Give the preparation type.
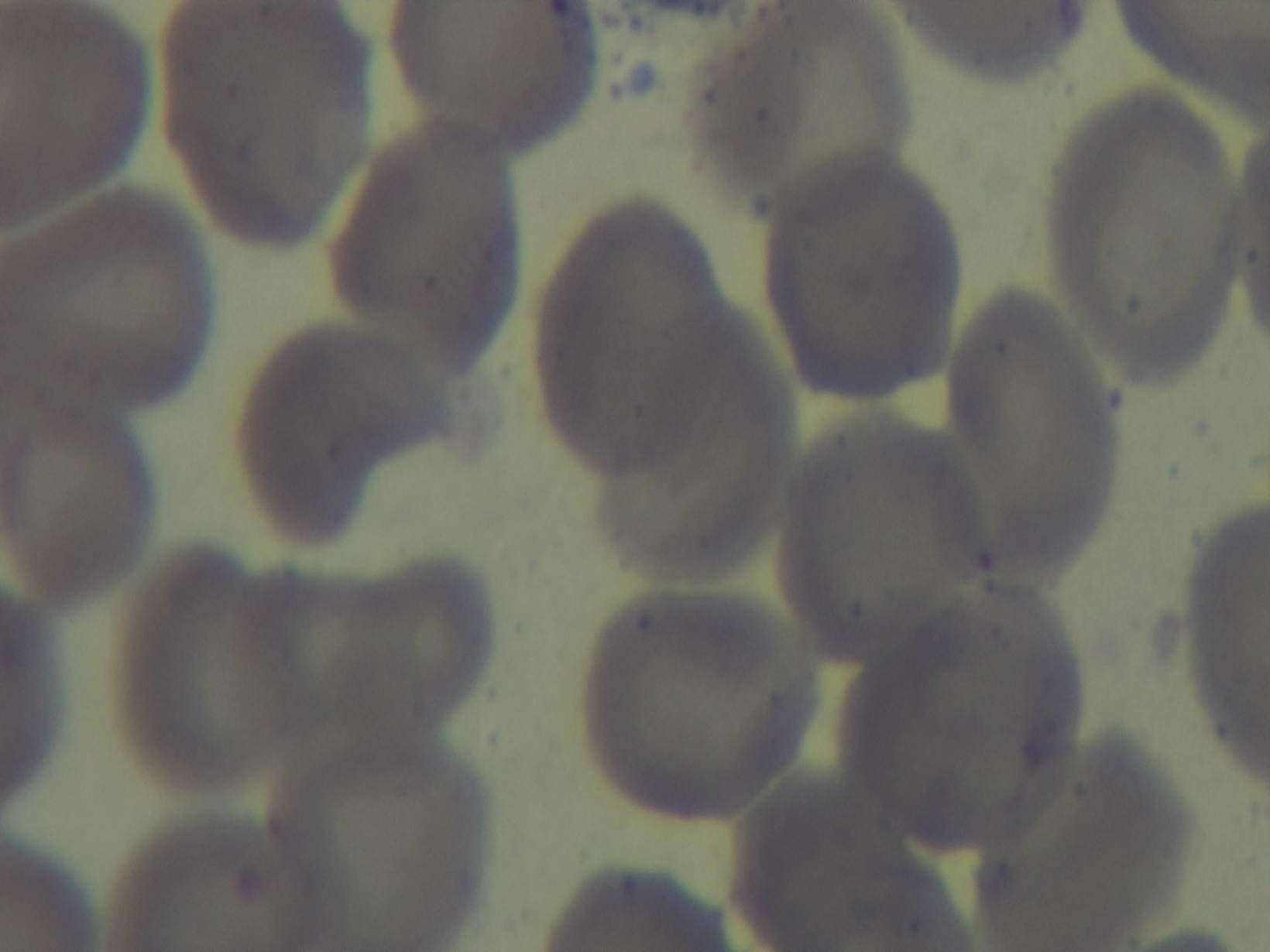
A thin smear.

Oil-immersion objective, 100x. Mounted 4K digital camera. Photomicrograph. Giemsa-stained. Malaria status: negative. Single field of view.